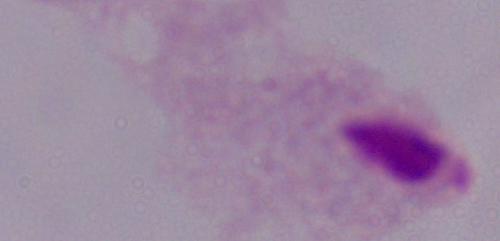
modality = photomicrograph
identification = trichomonad
magnification = 1000x